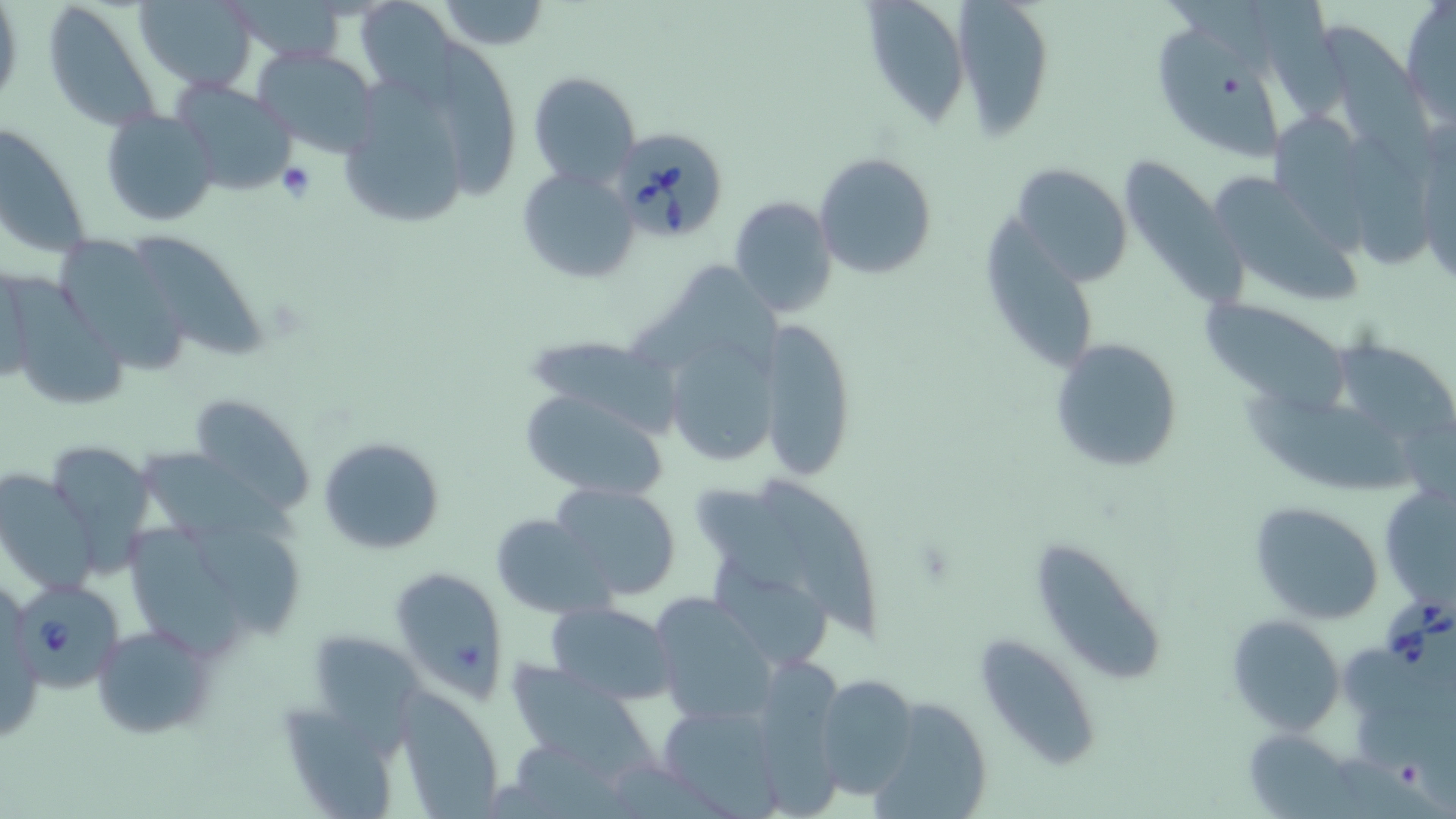
Summary:
  - Coordinate format: approximate bounding boxes as named x1/y1/x2/y2 corners in pixels
  - Platelet locations: (x1=276, y1=160, x2=316, y2=203)
  - Babesia divergens-infected red blood cell locations: (x1=609, y1=125, x2=729, y2=244), (x1=14, y1=580, x2=125, y2=693), (x1=1382, y1=596, x2=1455, y2=693)
  - Uninfected red blood cell locations: (x1=134, y1=0, x2=257, y2=90), (x1=433, y1=0, x2=551, y2=50), (x1=862, y1=0, x2=972, y2=124), (x1=947, y1=0, x2=1057, y2=130), (x1=40, y1=2, x2=163, y2=133), (x1=226, y1=2, x2=346, y2=68), (x1=1254, y1=2, x2=1359, y2=118), (x1=1400, y1=4, x2=1455, y2=127), (x1=1325, y1=25, x2=1444, y2=181), (x1=1158, y1=29, x2=1285, y2=159), (x1=438, y1=38, x2=521, y2=201), (x1=252, y1=46, x2=381, y2=158), (x1=529, y1=71, x2=640, y2=190), (x1=170, y1=79, x2=299, y2=197), (x1=346, y1=79, x2=464, y2=224), (x1=101, y1=108, x2=219, y2=228), (x1=1268, y1=110, x2=1379, y2=258), (x1=0, y1=122, x2=91, y2=259), (x1=1345, y1=134, x2=1441, y2=276), (x1=1417, y1=134, x2=1455, y2=290), (x1=814, y1=153, x2=938, y2=280), (x1=1118, y1=155, x2=1246, y2=303), (x1=1009, y1=162, x2=1134, y2=286), (x1=516, y1=165, x2=639, y2=284), (x1=1208, y1=175, x2=1364, y2=301), (x1=729, y1=196, x2=840, y2=319), (x1=986, y1=217, x2=1094, y2=369), (x1=60, y1=236, x2=189, y2=379), (x1=133, y1=236, x2=272, y2=363), (x1=629, y1=262, x2=786, y2=360), (x1=7, y1=277, x2=131, y2=410), (x1=1196, y1=294, x2=1355, y2=411), (x1=759, y1=316, x2=857, y2=481), (x1=660, y1=329, x2=782, y2=470), (x1=1338, y1=334, x2=1456, y2=435), (x1=1050, y1=337, x2=1185, y2=472), (x1=526, y1=338, x2=680, y2=444), (x1=518, y1=387, x2=669, y2=498), (x1=1245, y1=394, x2=1418, y2=491), (x1=188, y1=395, x2=313, y2=514), (x1=318, y1=435, x2=445, y2=556), (x1=40, y1=441, x2=156, y2=572), (x1=138, y1=451, x2=307, y2=550), (x1=0, y1=469, x2=97, y2=595), (x1=763, y1=480, x2=879, y2=643), (x1=546, y1=481, x2=684, y2=602), (x1=696, y1=484, x2=818, y2=603), (x1=1381, y1=484, x2=1455, y2=606), (x1=1249, y1=500, x2=1385, y2=624), (x1=487, y1=513, x2=616, y2=618), (x1=181, y1=517, x2=305, y2=634), (x1=126, y1=527, x2=245, y2=661), (x1=1035, y1=542, x2=1164, y2=688), (x1=712, y1=562, x2=834, y2=666), (x1=391, y1=568, x2=510, y2=700), (x1=649, y1=593, x2=778, y2=725), (x1=544, y1=599, x2=674, y2=706), (x1=1227, y1=615, x2=1344, y2=735), (x1=92, y1=625, x2=216, y2=737), (x1=977, y1=632, x2=1102, y2=771), (x1=321, y1=641, x2=423, y2=755), (x1=764, y1=655, x2=853, y2=819), (x1=508, y1=666, x2=660, y2=786), (x1=814, y1=672, x2=919, y2=799), (x1=392, y1=683, x2=504, y2=819), (x1=872, y1=692, x2=996, y2=819), (x1=285, y1=702, x2=395, y2=814), (x1=657, y1=703, x2=785, y2=812), (x1=1243, y1=728, x2=1355, y2=817)
  - Slide-level diagnosis: Babesia divergens
  - Field of view: one of a larger specimen
  - Stain: May-Grünwald-Giemsa
  - Image size: 1456×819 pixels
  - Magnification: 1000x
  - Modality: optical microscopy
  - Preparation: thin blood film